State which cell type is depicted.
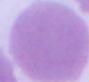

This is an erythrocyte.

Summary:
  - Magnification: 1000x
  - Modality: photomicrograph